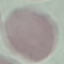

malaria status = uninfected
image type = automatically extracted cell patch, resized to 64 × 64 pixels
preparation = thin blood smear
capture = smartphone camera at the microscope eyepiece
stain = Giemsa